State the blood parasite species.
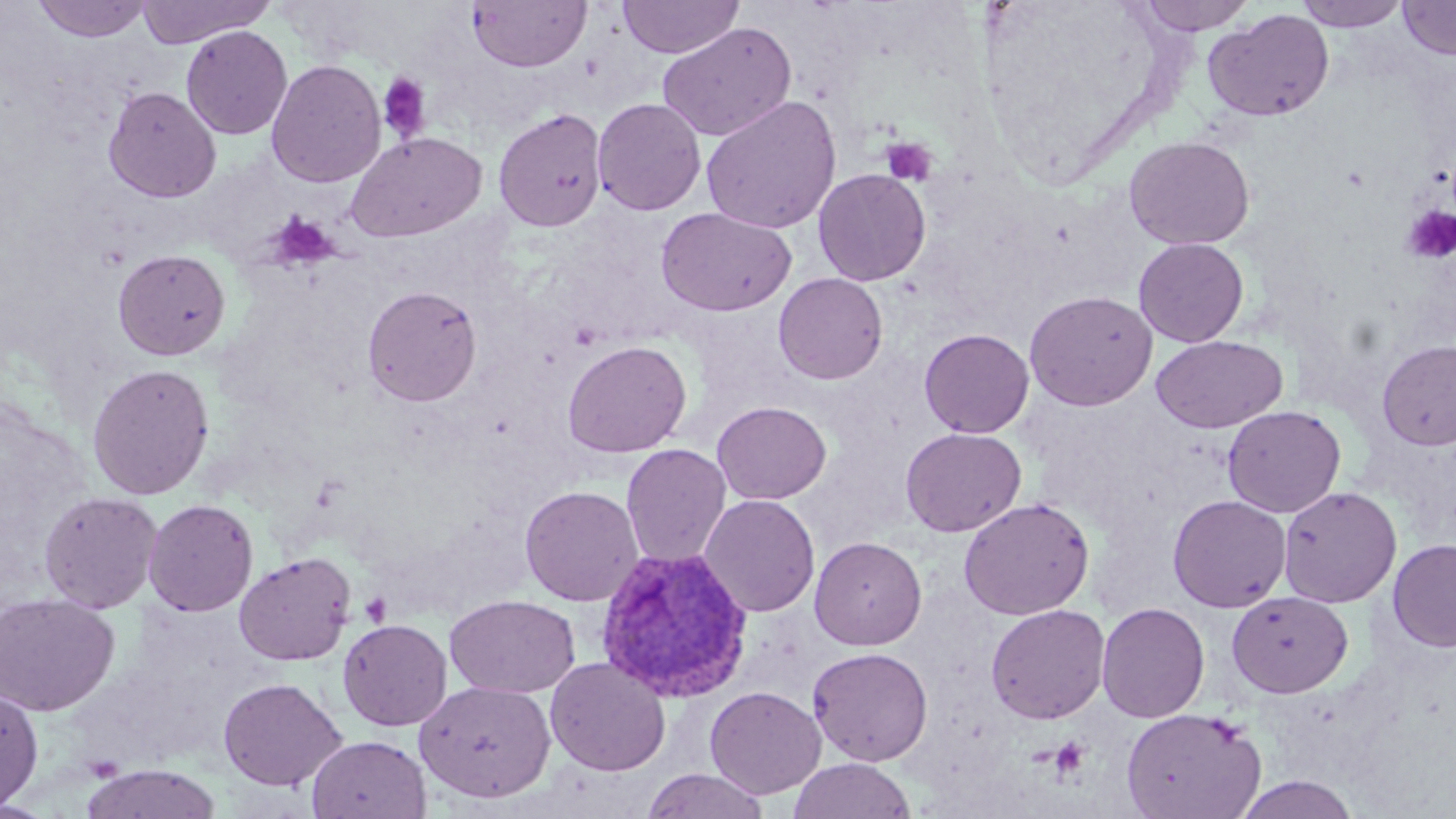

Plasmodium vivax.

Summary:
  - Coordinate format: approximate bounding boxes as named x1/y1/x2/y2 corners in pixels
  - Uninfected red blood cell locations: (x1=31, y1=0, x2=152, y2=42), (x1=135, y1=0, x2=275, y2=47), (x1=617, y1=0, x2=743, y2=59), (x1=1133, y1=0, x2=1258, y2=34), (x1=1294, y1=0, x2=1408, y2=31), (x1=1398, y1=0, x2=1456, y2=60), (x1=467, y1=1, x2=591, y2=72), (x1=1203, y1=8, x2=1335, y2=122), (x1=657, y1=21, x2=797, y2=143), (x1=180, y1=26, x2=293, y2=140), (x1=266, y1=59, x2=386, y2=188), (x1=103, y1=86, x2=222, y2=203), (x1=701, y1=95, x2=841, y2=234), (x1=592, y1=98, x2=706, y2=216), (x1=493, y1=107, x2=607, y2=232), (x1=345, y1=131, x2=487, y2=243), (x1=1124, y1=136, x2=1255, y2=250), (x1=813, y1=169, x2=931, y2=286), (x1=656, y1=207, x2=795, y2=317), (x1=1133, y1=237, x2=1249, y2=347), (x1=112, y1=248, x2=231, y2=360), (x1=773, y1=273, x2=888, y2=384), (x1=362, y1=284, x2=482, y2=407), (x1=1023, y1=290, x2=1158, y2=411), (x1=919, y1=328, x2=1034, y2=438), (x1=1151, y1=335, x2=1287, y2=433), (x1=1376, y1=339, x2=1456, y2=450), (x1=562, y1=340, x2=691, y2=457), (x1=86, y1=362, x2=215, y2=500), (x1=711, y1=400, x2=832, y2=505), (x1=1223, y1=405, x2=1346, y2=517), (x1=900, y1=427, x2=1027, y2=537), (x1=621, y1=443, x2=732, y2=569), (x1=520, y1=485, x2=644, y2=607), (x1=1278, y1=485, x2=1402, y2=607), (x1=38, y1=490, x2=163, y2=613), (x1=699, y1=494, x2=820, y2=617), (x1=1168, y1=494, x2=1291, y2=612), (x1=959, y1=497, x2=1095, y2=620), (x1=143, y1=498, x2=259, y2=617), (x1=810, y1=536, x2=927, y2=650), (x1=1387, y1=539, x2=1456, y2=652), (x1=234, y1=552, x2=355, y2=665), (x1=1227, y1=591, x2=1353, y2=698), (x1=0, y1=592, x2=120, y2=715), (x1=445, y1=594, x2=580, y2=698), (x1=1096, y1=602, x2=1210, y2=723), (x1=986, y1=604, x2=1110, y2=724), (x1=338, y1=619, x2=452, y2=731), (x1=807, y1=646, x2=933, y2=766), (x1=545, y1=657, x2=670, y2=775), (x1=218, y1=677, x2=347, y2=791), (x1=415, y1=680, x2=556, y2=803), (x1=0, y1=682, x2=44, y2=811), (x1=705, y1=686, x2=826, y2=799), (x1=1120, y1=706, x2=1267, y2=819), (x1=306, y1=734, x2=431, y2=819), (x1=787, y1=757, x2=917, y2=819), (x1=80, y1=763, x2=222, y2=819), (x1=640, y1=768, x2=770, y2=819), (x1=1233, y1=774, x2=1360, y2=818)
  - Plasmodium vivax-infected red blood cell locations: (x1=595, y1=546, x2=753, y2=701)
  - Platelet locations: (x1=376, y1=73, x2=433, y2=143), (x1=881, y1=138, x2=938, y2=186), (x1=1401, y1=206, x2=1456, y2=263), (x1=269, y1=213, x2=338, y2=269), (x1=359, y1=591, x2=392, y2=628), (x1=1048, y1=736, x2=1091, y2=781)
  - Field of view: single
  - Magnification: 1000x
  - Image size: 1456×819 pixels
  - Preparation: thin blood smear
  - Modality: optical microscopy
  - Stain: May-Grünwald-Giemsa